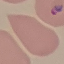
malaria status = uninfected
image type = cell patch, automatically extracted from a larger field of view and resized to 64 × 64 pixels
preparation = thin blood smear
stain = Giemsa
capture = smartphone through the microscope eyepiece